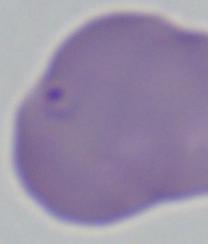
identification = Babesia
magnification = 1000x
modality = photomicrograph